State the blood parasite species.
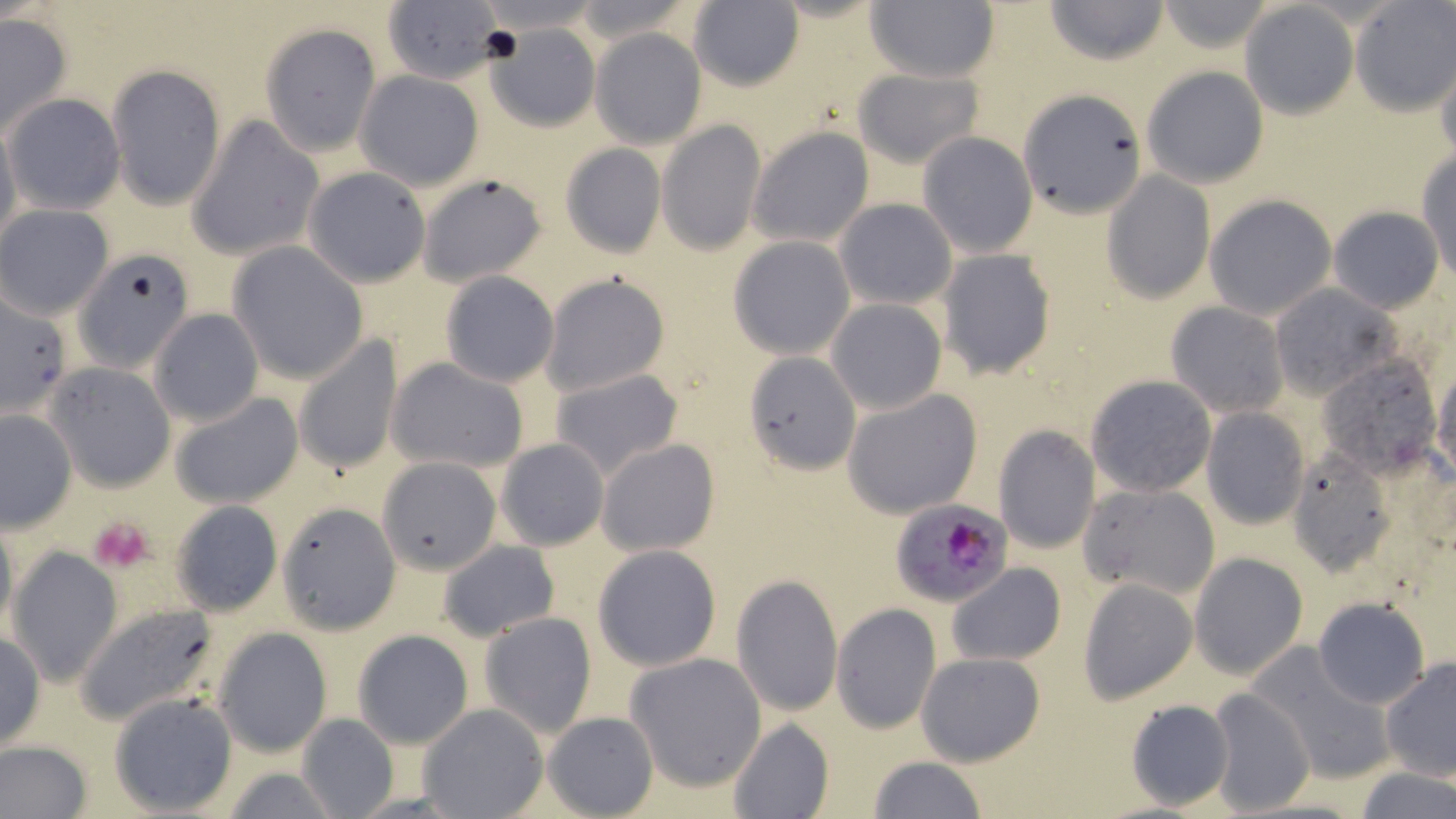

Plasmodium falciparum.

magnification = 1000x
Plasmodium falciparum-infected red blood cell locations = approximate bounding boxes as [x1, y1, x2, y2] in pixels: [892, 498, 1012, 606]
modality = optical microscopy
preparation = thin blood film
uninfected red blood cell locations = approximate bounding boxes as [x1, y1, x2, y2] in pixels: [1044, 0, 1170, 66], [380, 1, 505, 86], [686, 1, 805, 90], [863, 1, 1000, 84], [1155, 1, 1276, 52], [1240, 3, 1358, 119], [1352, 3, 1456, 115], [0, 15, 73, 136], [485, 22, 600, 132], [260, 23, 382, 155], [590, 30, 707, 149], [1435, 56, 1456, 164], [106, 64, 226, 211], [1140, 65, 1270, 189], [852, 67, 985, 168], [356, 71, 483, 191], [1020, 88, 1149, 215], [5, 93, 125, 214], [0, 115, 22, 255], [188, 117, 324, 261], [658, 121, 766, 255], [748, 126, 875, 248], [917, 131, 1039, 258], [559, 144, 667, 258], [1417, 149, 1456, 283], [305, 166, 431, 287], [418, 173, 548, 287], [1102, 173, 1214, 302], [1204, 193, 1339, 320], [834, 197, 957, 309], [1, 206, 113, 318], [1328, 206, 1445, 313], [727, 236, 856, 359], [227, 244, 368, 384], [938, 250, 1057, 382], [75, 252, 197, 374], [438, 271, 559, 388], [541, 273, 672, 397], [1270, 284, 1401, 399], [0, 293, 74, 420], [825, 299, 947, 416], [1165, 302, 1289, 419], [149, 309, 265, 427], [294, 336, 404, 476], [743, 350, 863, 473], [1318, 354, 1442, 478], [388, 356, 529, 474], [47, 362, 176, 492], [549, 368, 684, 482], [1432, 370, 1455, 485], [1085, 374, 1217, 497], [843, 388, 985, 518], [171, 390, 303, 509], [1201, 407, 1311, 529], [1, 409, 76, 532], [993, 425, 1101, 554], [495, 438, 610, 551], [597, 438, 720, 558], [1288, 447, 1398, 575], [376, 455, 503, 575], [1080, 482, 1218, 603], [171, 500, 283, 616], [277, 503, 399, 632], [0, 513, 18, 643], [436, 540, 560, 642], [7, 545, 124, 687], [593, 545, 722, 671], [1190, 551, 1308, 680], [947, 564, 1066, 666], [730, 574, 844, 716], [1078, 579, 1198, 704], [1312, 598, 1428, 708], [73, 600, 225, 725], [832, 603, 941, 732], [479, 612, 598, 737], [213, 627, 333, 756], [353, 629, 473, 750], [0, 631, 45, 751], [1247, 645, 1395, 786], [916, 651, 1046, 768], [625, 652, 769, 792], [1379, 655, 1456, 781], [1206, 686, 1313, 817], [109, 692, 239, 815], [1124, 699, 1233, 811], [420, 703, 548, 818], [543, 711, 659, 819], [300, 712, 399, 819], [726, 719, 833, 819], [0, 740, 93, 819], [867, 755, 987, 819], [1353, 768, 1455, 819]
image size = 1456×819 pixels
field of view = single
platelet locations = approximate bounding boxes as [x1, y1, x2, y2] in pixels: [88, 517, 153, 574]
stain = May-Grünwald-Giemsa